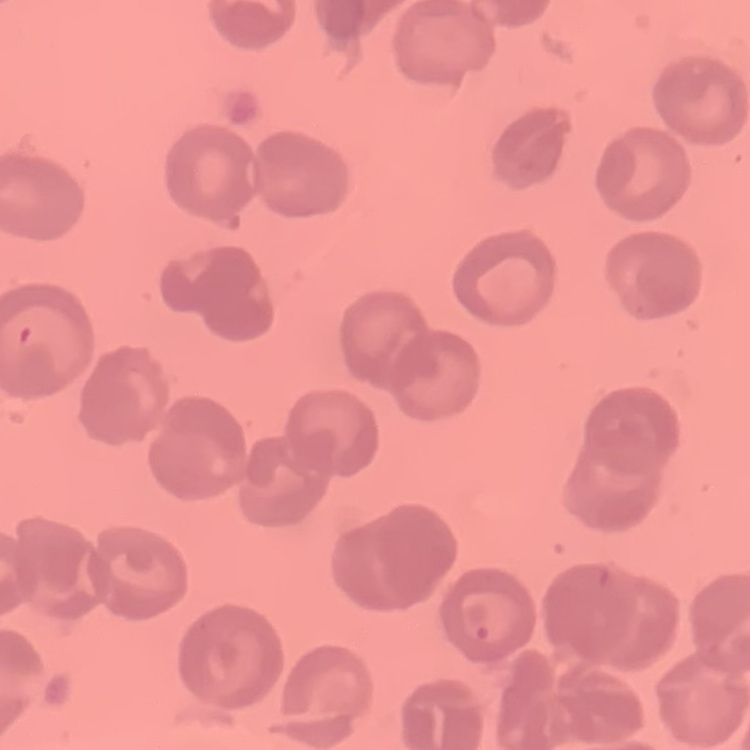 The erythrocytes show no rouleaux formation. One tile cut from a larger photomicrograph. Thin blood smear. Field's or Giemsa stain.